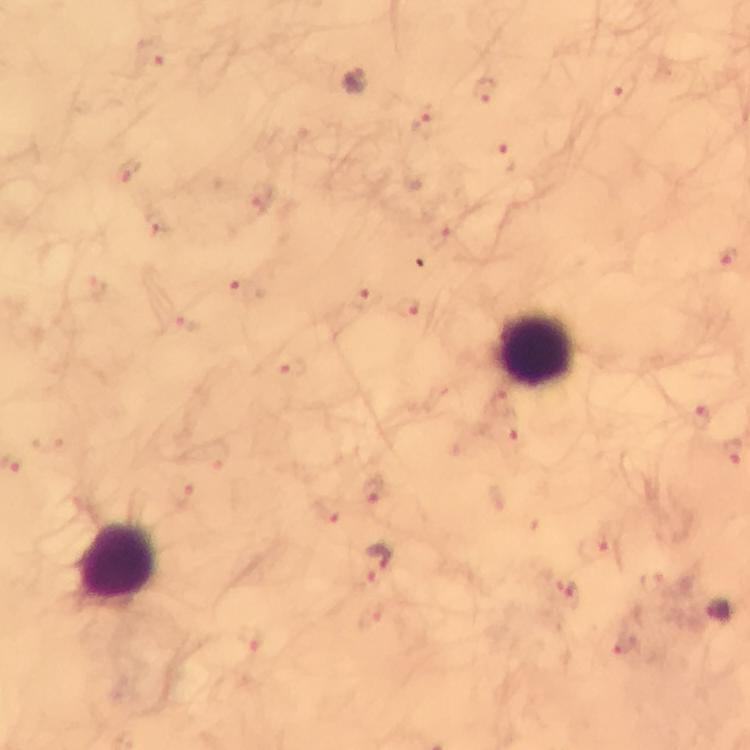

magnification: 100x
preparation: thick blood film
leukocyte_locations: 'approximate centers as {x, y} in pixels: {537, 348}, {120, 560}'
stain: Giemsa
plasmodium_parasite_locations: 'approximate centers as {x, y} in pixels: {355, 83}, {376, 562}, {721, 613}'
capture: smartphone mounted on the microscope
cropped_from: one field of view
image_size: 750×750 pixels
context: from a malaria diagnostic workup
immersion_oil: used